Identify the preparation type.
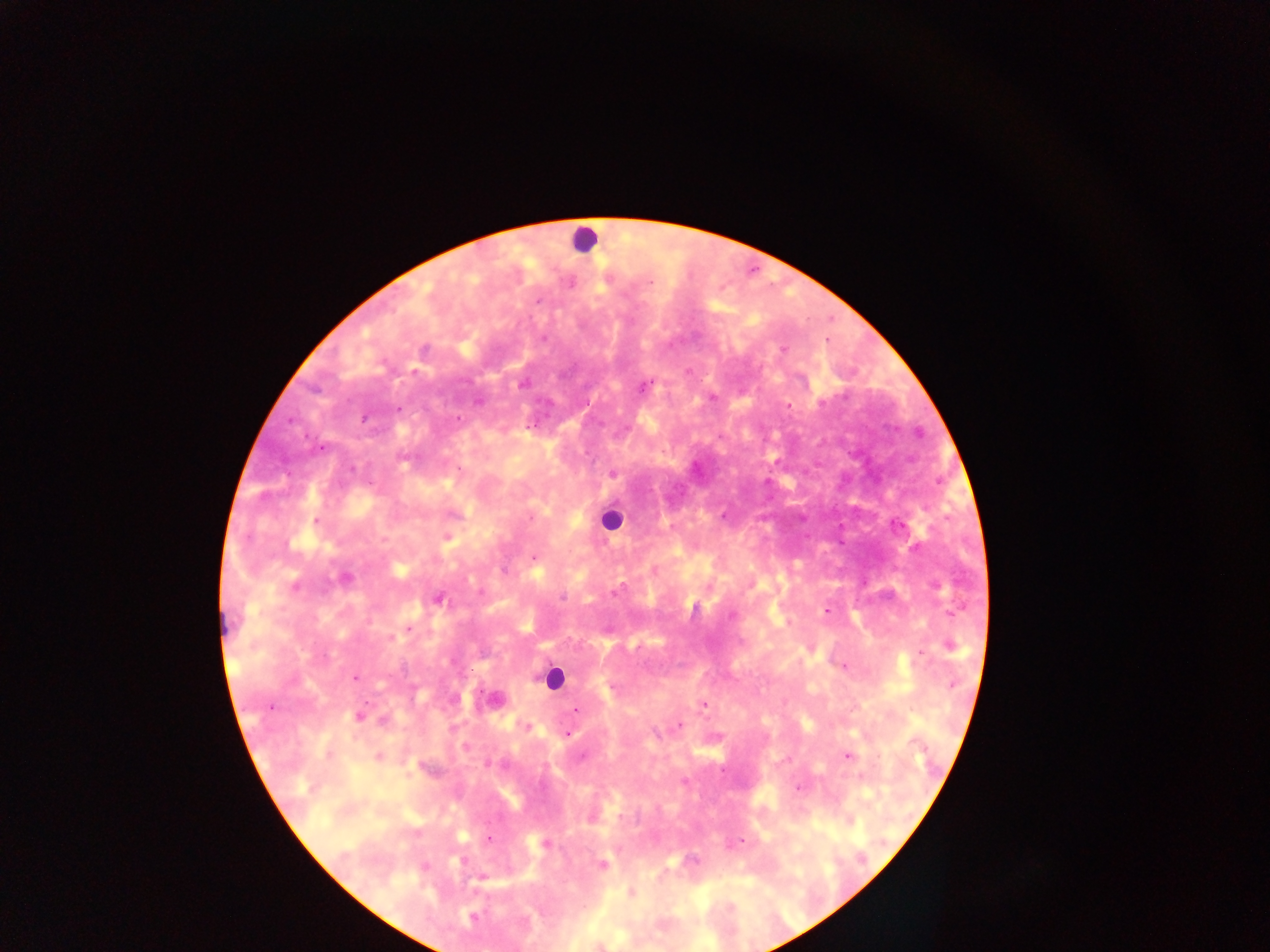
Thick blood film.

field of view = single
capture = mobile-phone photograph through a microscope
leukocyte locations = approximate centers as {x, y} in pixels: {584, 239}, {611, 519}, {552, 678}
Plasmodium parasite locations = approximate centers as {x, y} in pixels: {650, 282}, {537, 301}, {543, 339}, {424, 349}, {783, 350}, {414, 371}, {523, 383}, {642, 387}, {712, 397}, {478, 401}, {788, 406}, {398, 409}, {364, 418}, {458, 419}, {528, 426}, {322, 449}, {352, 468}, {612, 474}, {724, 516}, {531, 518}, {317, 521}, {447, 538}, {534, 557}, {504, 570}, {654, 571}, {345, 578}, {294, 586}, {615, 592}, {562, 598}, {438, 599}, {827, 611}, {732, 615}, {409, 629}, {392, 637}, {950, 646}, {921, 654}, {843, 667}, {355, 678}, {953, 684}, {494, 699}, {704, 705}, {270, 706}, {576, 710}, {359, 716}, {382, 720}, {679, 725}, {527, 727}, {655, 732}, {567, 734}, {464, 747}, {848, 755}, {379, 757}, {581, 757}, {490, 764}, {684, 782}, {490, 838}, {741, 841}, {545, 843}, {693, 860}, {602, 865}, {425, 866}, {481, 878}, {632, 894}, {472, 917}
image size = 1270×952 pixels
country = Ghana